Classify the preparation.
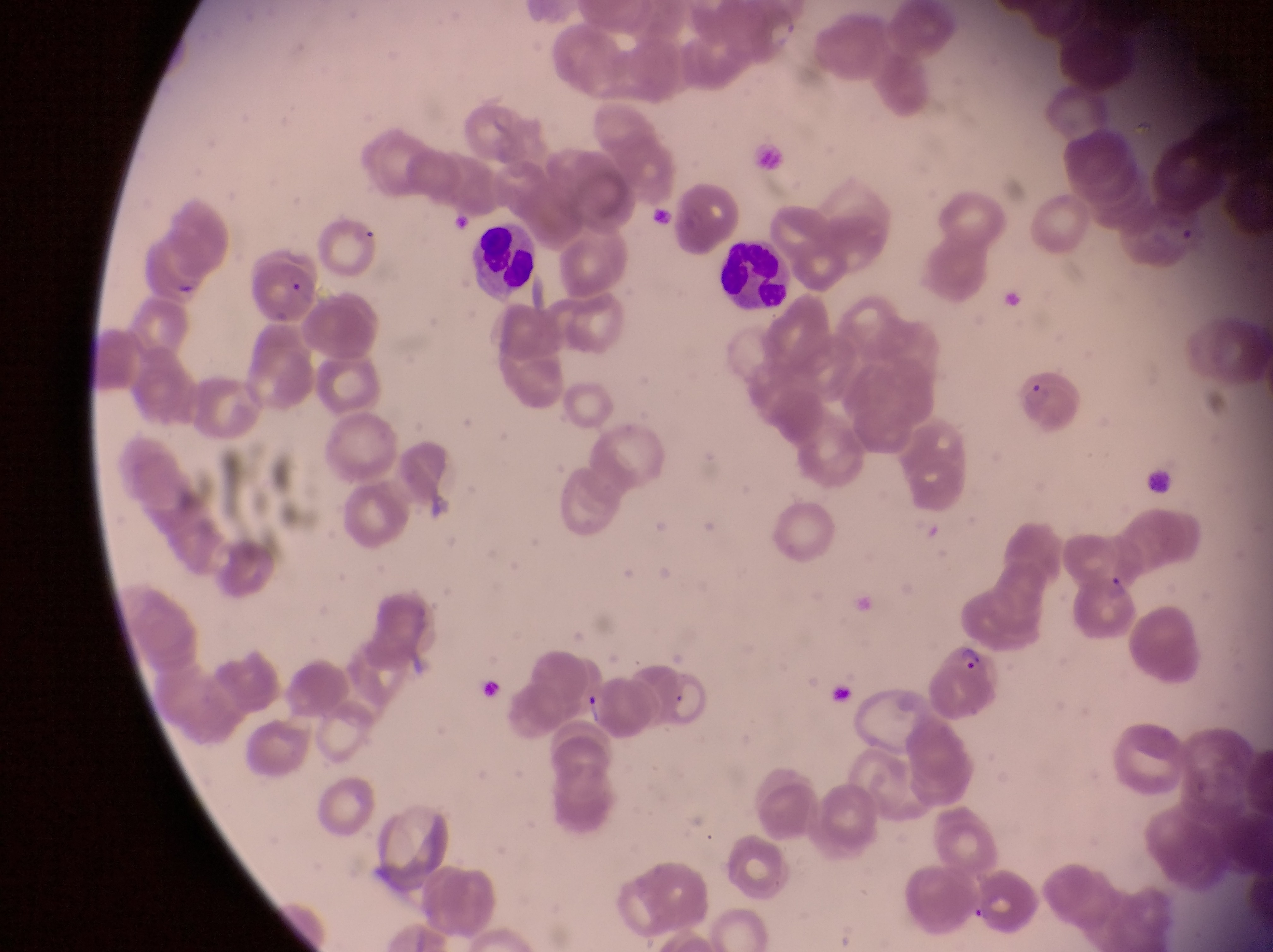
This is a thin smear.

Approximate bounding boxes as left top right bottom in pixels.
Summary:
  - Parasitised red blood cell locations: 1016 359 1078 434; 1073 570 1140 644; 919 639 1002 717
  - Leukocyte locations: 467 223 541 297; 721 235 794 310; 1146 467 1178 503
  - Artifact (platelet-like body, stain precipitate, or debris) locations: 251 259 318 314; 581 691 609 736
  - Image size: 1273×952 pixels
  - Capture: smartphone photograph through the eyepiece of an Olympus CX-23 microscope
  - Field of view: single
  - Country: Uganda
  - Magnification: 1000x